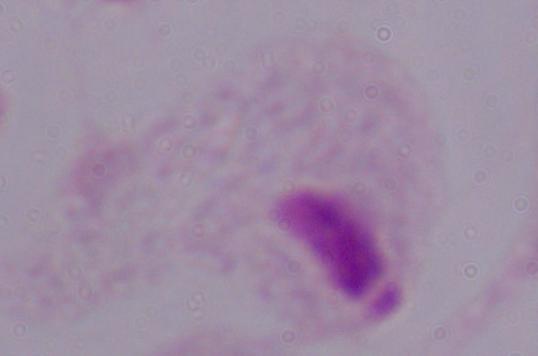
Summary:
  - Modality: micrograph
  - Identification: trichomonad
  - Magnification: 1000x